Assess the morphology of the red blood cells.
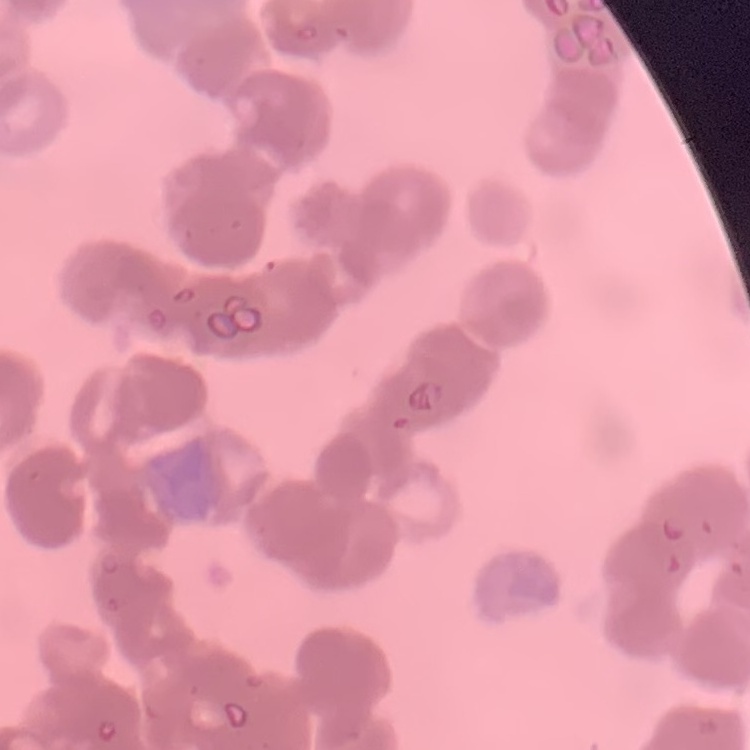

They show rouleaux formation.

preparation = thin blood film
stain = Field's or Giemsa
image type = square crop of a larger photomicrograph